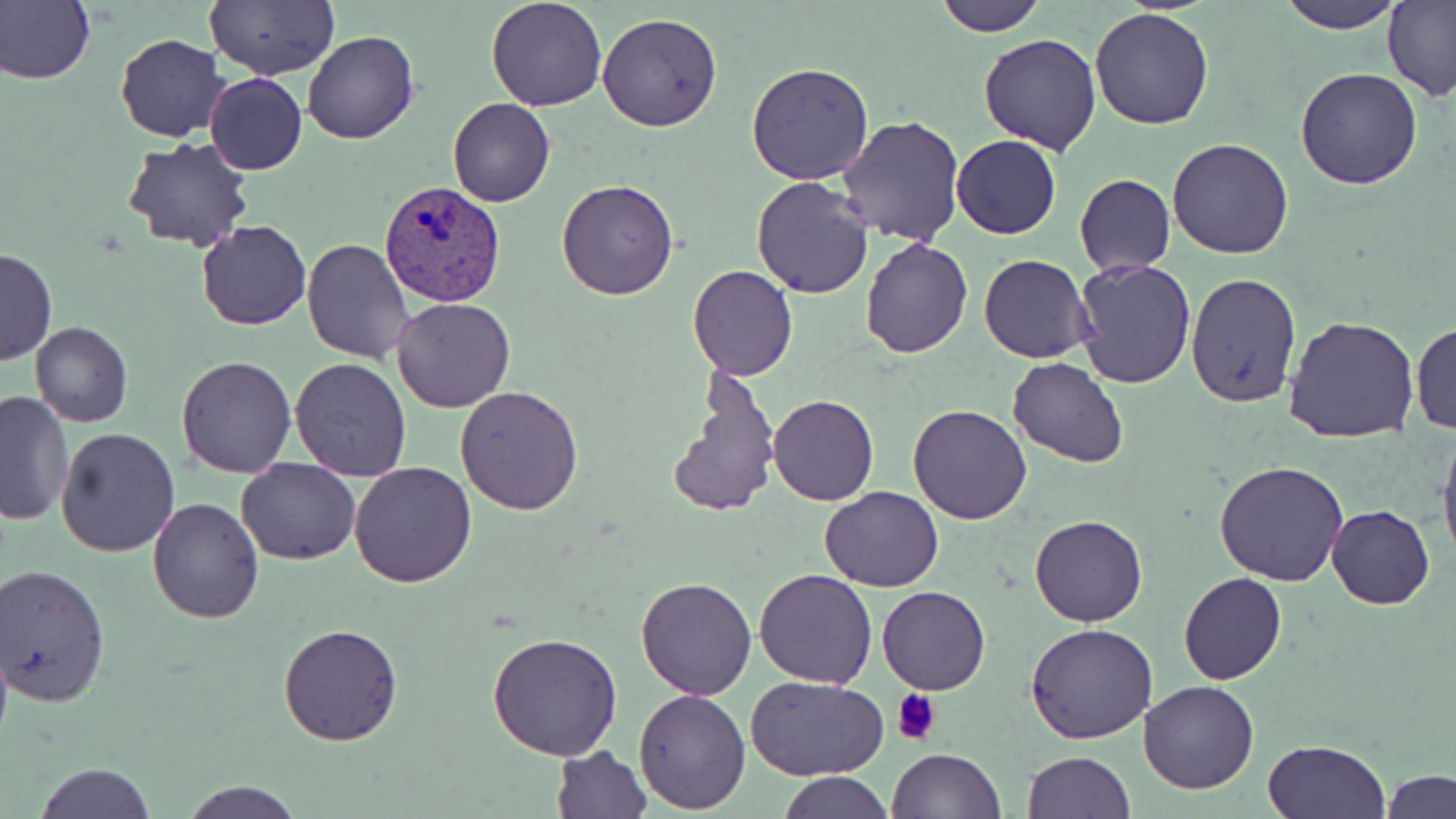
Summary:
  - Coordinate format: approximate bounding boxes as named x1/y1/x2/y2 corners in pixels
  - Plasmodium vivax-infected red blood cell locations: (x1=381, y1=182, x2=507, y2=306)
  - Uninfected red blood cell locations: (x1=0, y1=0, x2=94, y2=85), (x1=206, y1=0, x2=338, y2=80), (x1=485, y1=0, x2=608, y2=111), (x1=934, y1=0, x2=1047, y2=37), (x1=1279, y1=0, x2=1405, y2=32), (x1=1383, y1=0, x2=1456, y2=103), (x1=1090, y1=7, x2=1215, y2=129), (x1=597, y1=12, x2=724, y2=131), (x1=303, y1=30, x2=418, y2=144), (x1=979, y1=32, x2=1104, y2=154), (x1=116, y1=34, x2=230, y2=143), (x1=748, y1=64, x2=875, y2=185), (x1=1294, y1=67, x2=1423, y2=189), (x1=205, y1=72, x2=308, y2=175), (x1=447, y1=96, x2=555, y2=207), (x1=838, y1=116, x2=967, y2=247), (x1=951, y1=135, x2=1061, y2=239), (x1=1168, y1=137, x2=1295, y2=258), (x1=124, y1=138, x2=255, y2=254), (x1=1075, y1=174, x2=1174, y2=275), (x1=751, y1=176, x2=874, y2=298), (x1=555, y1=178, x2=679, y2=300), (x1=197, y1=221, x2=310, y2=331), (x1=860, y1=237, x2=973, y2=357), (x1=301, y1=239, x2=415, y2=365), (x1=0, y1=249, x2=56, y2=366), (x1=979, y1=254, x2=1096, y2=364), (x1=1072, y1=261, x2=1197, y2=389), (x1=687, y1=266, x2=799, y2=380), (x1=1186, y1=274, x2=1302, y2=409), (x1=392, y1=297, x2=515, y2=414), (x1=1284, y1=314, x2=1420, y2=445), (x1=30, y1=321, x2=132, y2=428), (x1=1410, y1=322, x2=1455, y2=435), (x1=176, y1=355, x2=298, y2=477), (x1=289, y1=357, x2=413, y2=481), (x1=1007, y1=358, x2=1129, y2=468), (x1=667, y1=368, x2=779, y2=519), (x1=455, y1=387, x2=584, y2=516), (x1=0, y1=389, x2=76, y2=526), (x1=767, y1=394, x2=878, y2=507), (x1=907, y1=404, x2=1033, y2=525), (x1=56, y1=427, x2=180, y2=557), (x1=1438, y1=431, x2=1456, y2=569), (x1=236, y1=457, x2=361, y2=565), (x1=349, y1=461, x2=476, y2=587), (x1=1214, y1=462, x2=1350, y2=587), (x1=821, y1=487, x2=943, y2=592), (x1=147, y1=496, x2=265, y2=622), (x1=1326, y1=506, x2=1434, y2=609), (x1=1029, y1=513, x2=1149, y2=627), (x1=1, y1=564, x2=112, y2=705), (x1=753, y1=569, x2=878, y2=689), (x1=1179, y1=573, x2=1286, y2=686), (x1=636, y1=575, x2=758, y2=699), (x1=876, y1=585, x2=991, y2=695), (x1=278, y1=623, x2=404, y2=745), (x1=1025, y1=623, x2=1158, y2=744), (x1=487, y1=631, x2=623, y2=759), (x1=748, y1=676, x2=887, y2=782), (x1=1136, y1=680, x2=1259, y2=795), (x1=635, y1=686, x2=751, y2=813), (x1=1263, y1=740, x2=1388, y2=819), (x1=551, y1=745, x2=652, y2=818), (x1=886, y1=749, x2=1006, y2=818), (x1=1022, y1=752, x2=1135, y2=818), (x1=30, y1=762, x2=157, y2=819), (x1=1381, y1=769, x2=1455, y2=818), (x1=778, y1=773, x2=894, y2=818), (x1=180, y1=780, x2=304, y2=819)
  - Platelet locations: (x1=891, y1=688, x2=944, y2=743)
  - Slide-level diagnosis: Plasmodium vivax
  - Preparation: thin blood film
  - Image size: 1456×819 pixels
  - Field of view: one of a larger specimen
  - Stain: May-Grünwald-Giemsa
  - Magnification: 1000x
  - Modality: optical microscopy